Classify this cell by malaria status.
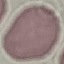
Uninfected.

Photographed with a smartphone camera at the microscope eyepiece. Cell patch, automatically extracted from a larger field of view and resized to 64 × 64 pixels. Thin blood smear. Giemsa-stained preparation.